Classify this cell by malaria status.
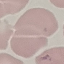

Parasitized.

Giemsa stain. Thin blood smear. Cell patch, automatically extracted from a larger field of view and resized to 64 × 64 pixels. Acquired by smartphone through the microscope eyepiece.